Look for Plasmodium parasites.
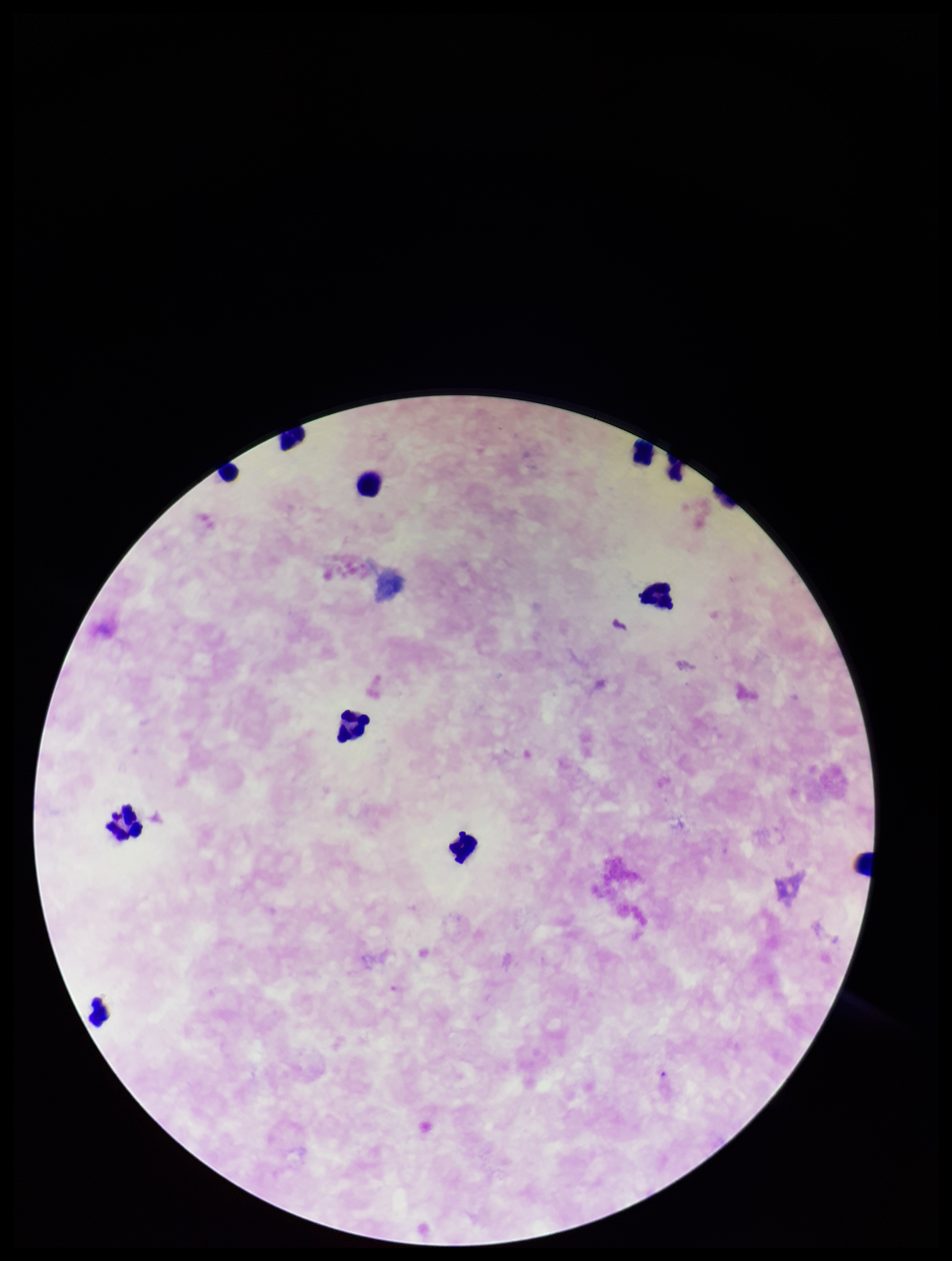
None seen.

image_size: 952×1261 pixels
leukocyte_count: 9
parasite_count: 0
preparation: thick smear
patient_malaria_status: negative
field_of_view: one from this slide
stain: Giemsa
capture: smartphone photograph through the microscope eyepiece